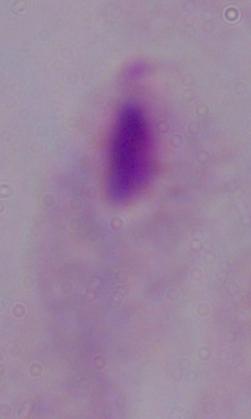

identification = trichomonad
modality = photomicrograph
magnification = 1000x